Assess this cell for malaria.
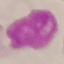
Uninfected.

Acquired by smartphone through the microscope eyepiece. Giemsa-stained preparation. Cell patch, automatically extracted from a larger field of view and resized to 64 × 64 pixels. Thin smear of blood.